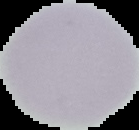

image type = segmented cell region with the area outside set to black
image size = 139×130 pixels
malaria status = uninfected
preparation = thin blood film